Name the parasite shown.
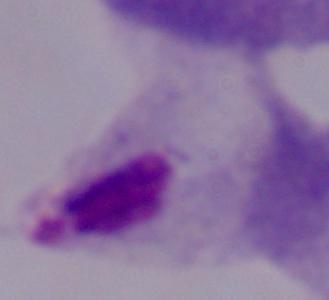

This is a trichomonad.

Photomicrograph. Captured at 1000x magnification.